Locate every Plasmodium parasite.
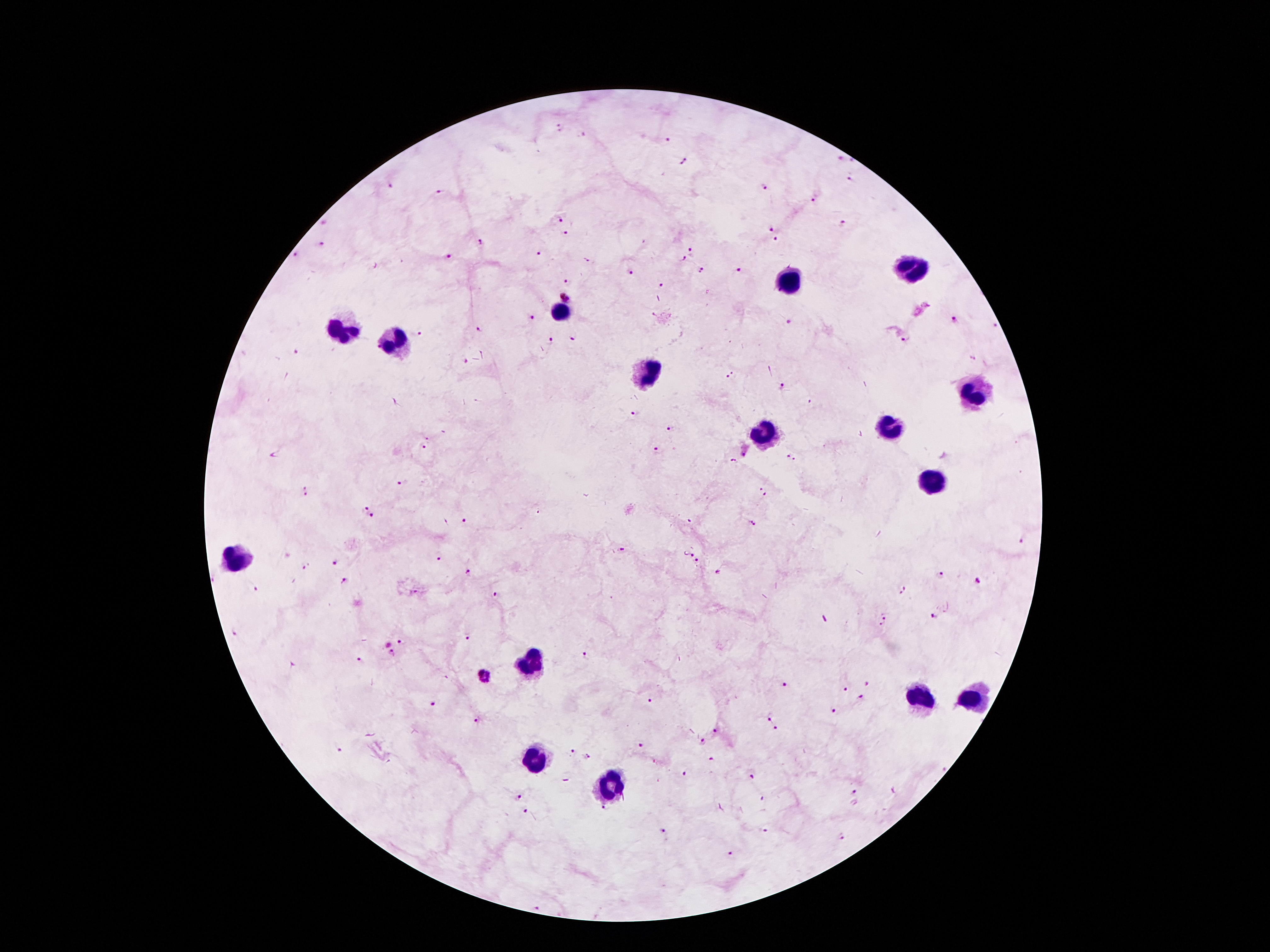
Approximate object centers, in pixels from the top-left corner.
Plasmodium parasites: (x=560, y=128), (x=581, y=135), (x=669, y=139), (x=838, y=158), (x=685, y=162), (x=851, y=180), (x=765, y=186), (x=392, y=187), (x=440, y=192), (x=813, y=200), (x=560, y=219), (x=844, y=223), (x=771, y=228), (x=566, y=232), (x=777, y=241), (x=480, y=243), (x=322, y=245), (x=692, y=250), (x=295, y=255), (x=540, y=255), (x=447, y=258), (x=685, y=261), (x=701, y=271), (x=739, y=271), (x=631, y=272), (x=568, y=282), (x=660, y=285), (x=567, y=297), (x=530, y=317), (x=954, y=319), (x=995, y=326), (x=479, y=330), (x=421, y=334), (x=574, y=337), (x=906, y=338), (x=550, y=340), (x=297, y=351), (x=973, y=358), (x=464, y=363), (x=731, y=375), (x=781, y=387), (x=812, y=401), (x=635, y=414), (x=671, y=429), (x=429, y=437), (x=426, y=446), (x=656, y=450), (x=746, y=455), (x=791, y=457), (x=733, y=462), (x=400, y=482), (x=308, y=491), (x=762, y=491), (x=365, y=509), (x=371, y=517), (x=463, y=521), (x=754, y=522), (x=1022, y=540), (x=622, y=550), (x=439, y=554), (x=693, y=555), (x=335, y=561), (x=697, y=563), (x=305, y=566), (x=468, y=573), (x=940, y=574), (x=215, y=578), (x=346, y=581), (x=978, y=581), (x=257, y=589), (x=904, y=591), (x=497, y=595), (x=935, y=615), (x=883, y=622), (x=234, y=634), (x=468, y=638), (x=401, y=640), (x=392, y=654), (x=586, y=657), (x=360, y=660), (x=485, y=677), (x=785, y=684), (x=845, y=690), (x=862, y=698), (x=651, y=702), (x=434, y=704), (x=835, y=712), (x=771, y=716), (x=477, y=719), (x=778, y=729), (x=717, y=731), (x=702, y=741), (x=641, y=745), (x=340, y=749), (x=570, y=750), (x=586, y=756), (x=711, y=759), (x=687, y=773), (x=753, y=777), (x=855, y=792), (x=517, y=798), (x=526, y=810), (x=603, y=810), (x=662, y=830), (x=763, y=831), (x=841, y=837), (x=730, y=855), (x=538, y=907).

Leukocyte locations: (x=910, y=271), (x=790, y=279), (x=561, y=312), (x=344, y=329), (x=393, y=345), (x=651, y=375), (x=975, y=395), (x=891, y=427), (x=765, y=438), (x=932, y=486), (x=237, y=559), (x=529, y=666), (x=921, y=698), (x=973, y=701), (x=535, y=762), (x=611, y=787). Patient malaria status: infected with Plasmodium falciparum. Thick blood film. Image is 1270×952 pixels. Single field of view. Giemsa-stained preparation. Smartphone photograph taken through the microscope eyepiece. 100x magnification.